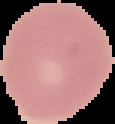
Summary:
  - Malaria status: uninfected
  - Preparation: thin blood smear
  - Image type: segmented cell region with the area outside set to black
  - Image size: 115×124 pixels